Locate every blood parasite and identify its species.
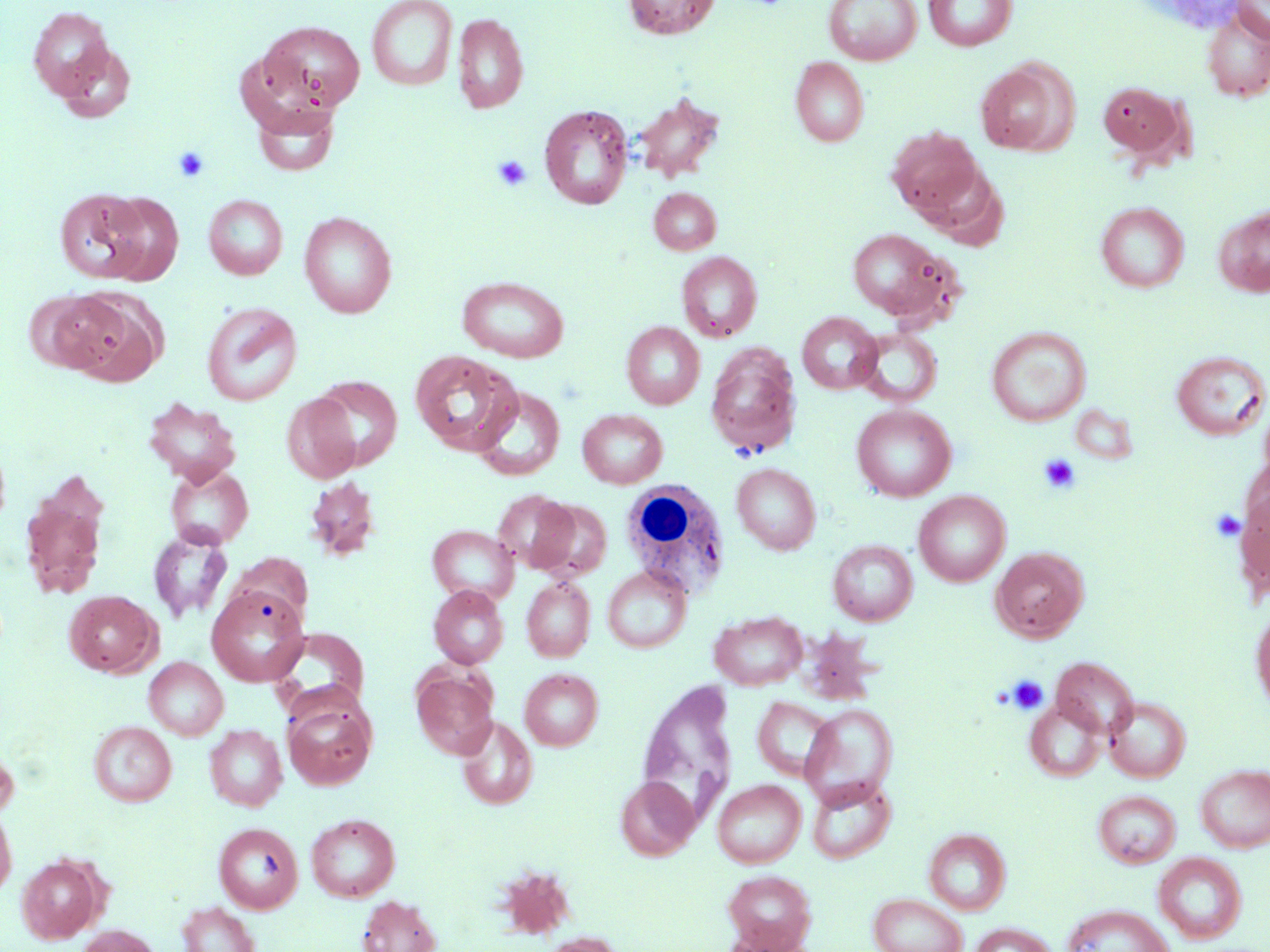

No blood parasites seen.

{
  "slide_level_diagnosis": "negative for blood parasites",
  "platelet_locations": "approximate bounding boxes as (x1,y1)-(x2,y2) corner pairs in pixels: (173,145)-(210,183), (492,154)-(531,192), (1038,454)-(1081,494), (1210,509)-(1246,542), (1006,675)-(1048,715)",
  "magnification": "1000x",
  "white_blood_cell_locations": "approximate bounding boxes as (x1,y1)-(x2,y2) corner pairs in pixels: (618,481)-(734,591)",
  "image_size": "1270×952 pixels",
  "field_of_view": "one of a larger specimen",
  "preparation": "thin blood film",
  "uninfected_red_blood_cell_locations": "approximate bounding boxes as (x1,y1)-(x2,y2) corner pairs in pixels: (367,0)-(458,91), (622,0)-(720,39), (824,0)-(922,65), (923,0)-(1018,51), (1232,0)-(1270,44), (28,6)-(116,101), (1201,9)-(1270,102), (453,13)-(529,114), (257,20)-(366,112), (51,42)-(137,123), (790,56)-(869,146), (975,61)-(1074,156), (1097,80)-(1186,160), (631,92)-(725,182), (252,103)-(339,176), (539,105)-(633,210), (886,126)-(983,219), (917,164)-(1008,248), (649,188)-(721,255), (55,189)-(150,283), (100,193)-(183,284), (203,194)-(288,280), (1095,201)-(1189,292), (1214,206)-(1270,297), (298,211)-(397,318), (846,229)-(951,321), (676,251)-(763,341), (457,276)-(569,362), (61,288)-(167,386), (23,290)-(120,373), (201,302)-(302,406), (798,312)-(882,393), (621,321)-(705,409), (986,325)-(1091,426), (854,328)-(943,407), (705,344)-(802,457), (409,350)-(519,454), (1170,351)-(1270,440), (312,375)-(402,469), (473,385)-(565,481), (282,393)-(362,483), (142,397)-(242,485), (851,404)-(956,502), (577,408)-(668,488), (164,463)-(254,549), (732,463)-(821,554), (19,475)-(109,601), (304,476)-(381,561), (493,489)-(578,574), (1235,489)-(1270,597), (914,491)-(1010,587), (530,499)-(612,581), (428,525)-(519,605), (148,531)-(233,623), (828,539)-(918,626), (991,546)-(1090,642), (229,553)-(313,627), (603,566)-(691,653), (521,577)-(595,661), (207,585)-(310,686), (428,585)-(508,668), (64,590)-(162,678), (1250,605)-(1270,714), (709,610)-(807,690), (270,627)-(370,716), (1051,656)-(1139,739), (144,657)-(228,740), (412,669)-(497,759), (520,669)-(603,750), (636,679)-(738,828), (282,694)-(376,791), (752,696)-(836,782), (1104,696)-(1191,782), (1025,699)-(1106,783), (800,703)-(898,809), (456,715)-(538,809), (89,721)-(176,806), (204,724)-(288,810), (0,731)-(20,820), (1196,764)-(1270,853), (615,776)-(700,860), (807,777)-(896,863), (712,779)-(806,867), (1093,790)-(1181,867), (0,801)-(17,899), (306,813)-(400,902), (214,823)-(303,914), (924,828)-(1011,915), (1153,852)-(1247,944), (17,853)-(104,943), (722,870)-(816,950), (868,892)-(968,952), (357,895)-(441,952), (177,901)-(260,952), (1062,904)-(1174,952), (969,922)-(1056,952), (75,925)-(160,952), (720,927)-(813,952), (539,933)-(624,952)",
  "modality": "optical microscopy",
  "stain": "May-Grünwald-Giemsa"
}